Outline each Plasmodium falciparum-infected red blood cell.
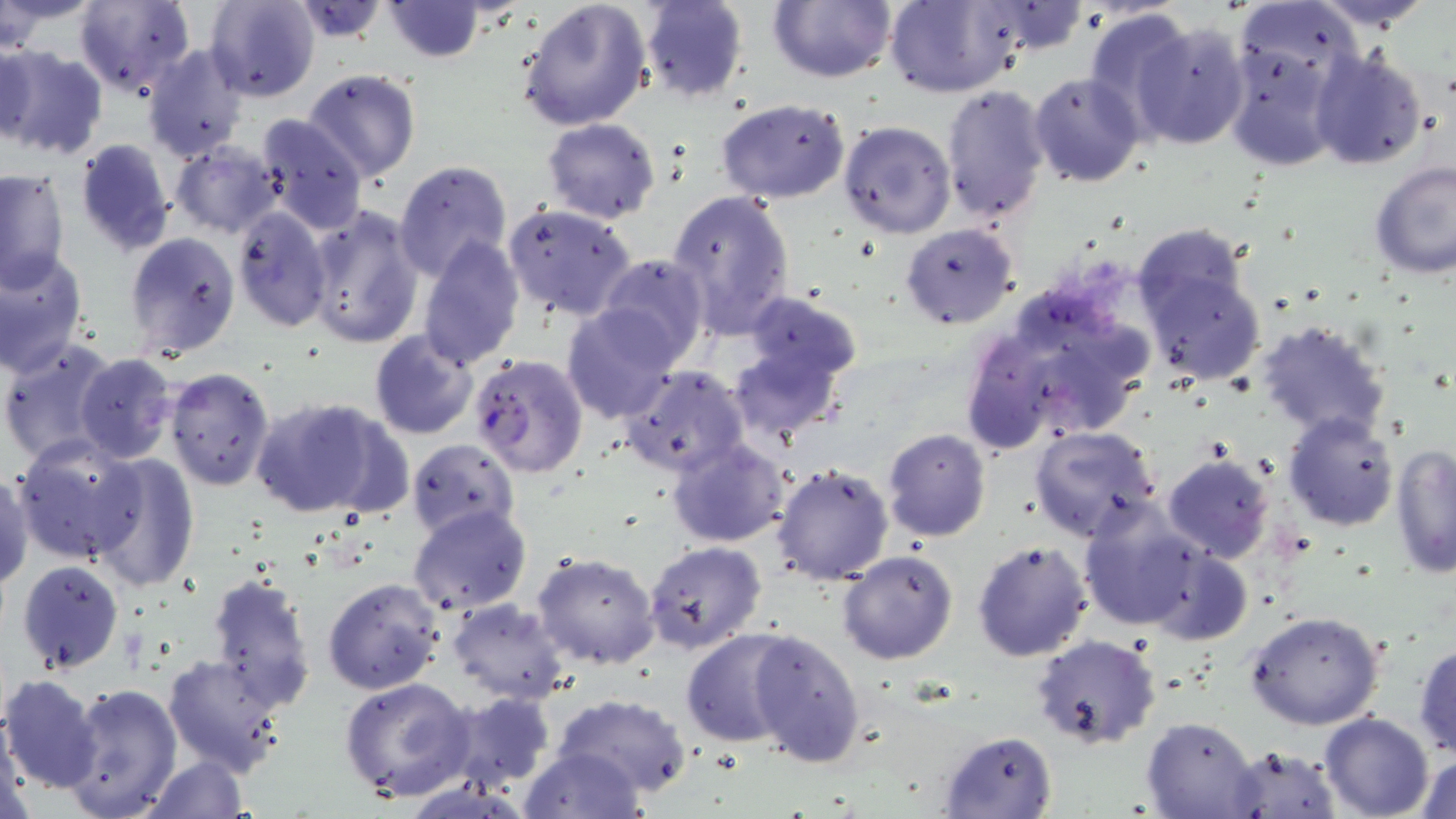

Approximate bounding boxes as (x1, y1, x2, y2) in pixels.
Plasmodium falciparum-infected red blood cells: (468, 354, 589, 479).

Uninfected red blood cell locations: (73, 0, 196, 97), (205, 0, 320, 103), (515, 0, 654, 132), (641, 0, 749, 104), (767, 0, 895, 84), (885, 0, 1025, 97), (1302, 0, 1445, 30), (969, 1, 1091, 58), (381, 2, 487, 63), (290, 3, 392, 46), (1084, 7, 1194, 131), (1132, 19, 1252, 150), (0, 35, 40, 144), (1223, 40, 1341, 171), (0, 43, 108, 160), (141, 45, 249, 163), (1308, 47, 1430, 172), (302, 68, 421, 185), (1029, 72, 1145, 188), (939, 84, 1052, 227), (715, 99, 851, 205), (255, 114, 369, 235), (541, 117, 661, 224), (838, 121, 957, 239), (74, 138, 177, 257), (169, 141, 286, 238), (393, 160, 512, 283), (1369, 161, 1455, 280), (0, 168, 69, 293), (665, 188, 796, 337), (502, 201, 638, 321), (304, 203, 425, 350), (231, 207, 333, 333), (900, 223, 1020, 329), (124, 231, 241, 359), (415, 238, 524, 371), (1135, 244, 1267, 384), (0, 249, 88, 377), (596, 253, 710, 366), (743, 291, 867, 380), (981, 293, 1159, 449), (562, 303, 684, 425), (1254, 317, 1392, 443), (369, 330, 479, 442), (957, 330, 1062, 455), (0, 339, 119, 469), (727, 344, 845, 444), (73, 353, 177, 462), (620, 364, 748, 477), (164, 366, 275, 491), (249, 396, 389, 518), (1282, 413, 1398, 531), (1028, 423, 1163, 541), (882, 429, 991, 543), (14, 437, 146, 562), (667, 438, 790, 548), (405, 439, 519, 541), (1390, 445, 1456, 577), (1161, 451, 1274, 563), (88, 455, 201, 593), (771, 463, 894, 585), (0, 470, 34, 591), (1076, 501, 1226, 637), (407, 504, 532, 617), (971, 539, 1093, 661), (642, 540, 767, 654), (1148, 546, 1251, 646), (837, 550, 959, 664), (532, 551, 659, 670), (16, 559, 123, 674), (207, 572, 316, 714), (322, 577, 445, 695), (446, 597, 570, 704), (1244, 608, 1386, 730), (748, 627, 867, 768), (681, 629, 801, 747), (1032, 634, 1162, 750), (1412, 638, 1456, 758), (162, 651, 289, 777), (1, 673, 104, 794), (339, 677, 478, 805), (62, 681, 182, 819), (444, 691, 557, 791), (551, 693, 693, 799), (1319, 711, 1435, 819), (1, 712, 28, 819), (1142, 715, 1259, 819), (939, 730, 1057, 817), (1223, 743, 1342, 818), (520, 745, 646, 819), (1412, 749, 1456, 819), (144, 754, 248, 819). Slide-level diagnosis: Plasmodium falciparum. Thin blood film. Light microscopy. Single field of view. May-Grünwald-Giemsa stain. 1000x magnification. Image is 1456×819 pixels.